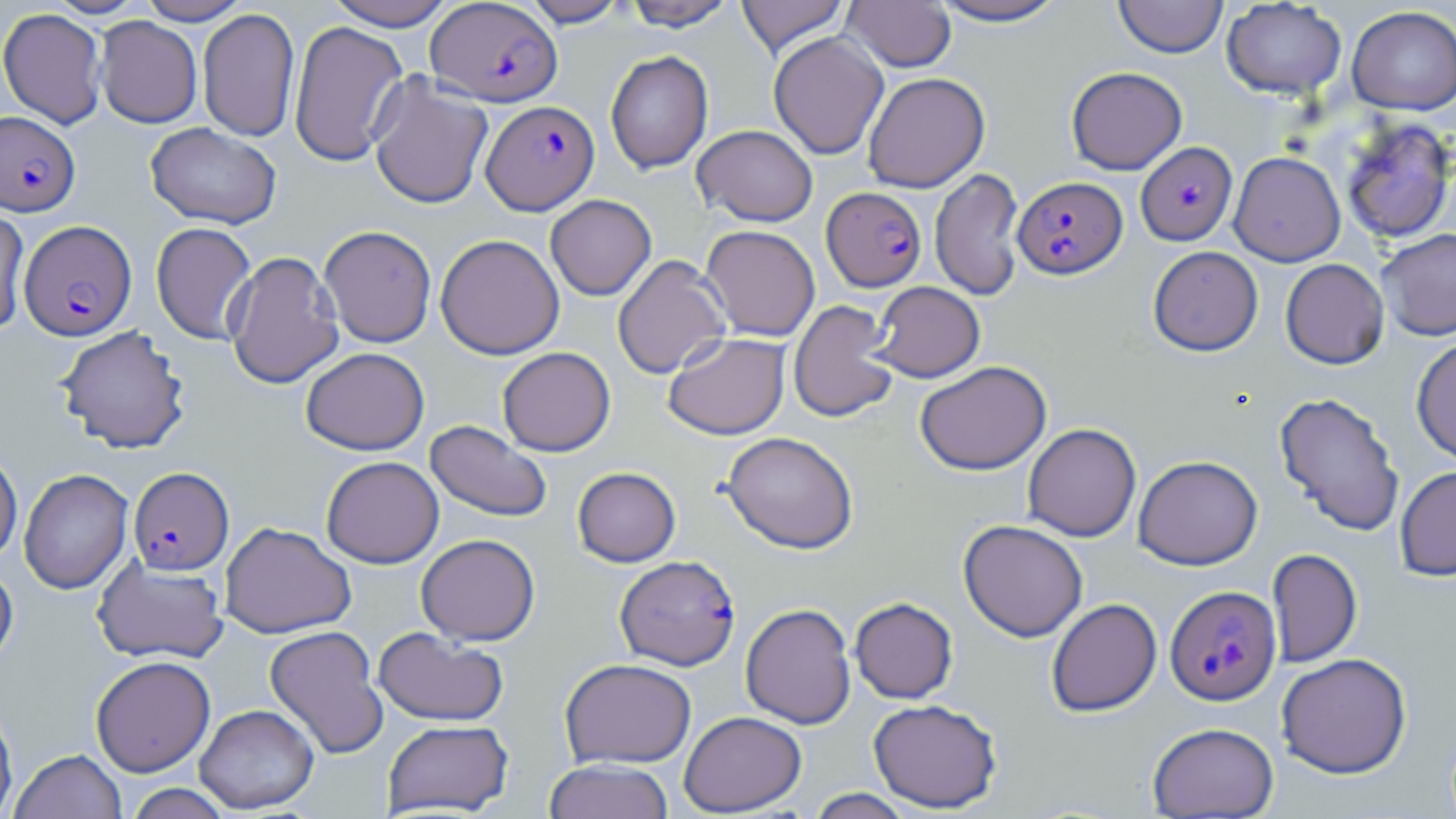

slide_level_diagnosis: Plasmodium falciparum
uninfected_red_blood_cell_locations: 'approximate bounding boxes as named x1/y1/x2/y2 corners in pixels: (x1=135, y1=0, x2=252, y2=25), (x1=324, y1=0, x2=459, y2=30), (x1=621, y1=0, x2=737, y2=30), (x1=736, y1=0, x2=850, y2=56), (x1=927, y1=0, x2=1071, y2=26), (x1=1113, y1=0, x2=1228, y2=58), (x1=521, y1=1, x2=630, y2=27), (x1=841, y1=1, x2=957, y2=73), (x1=1221, y1=1, x2=1347, y2=100), (x1=1347, y1=6, x2=1456, y2=115), (x1=0, y1=7, x2=107, y2=129), (x1=198, y1=8, x2=300, y2=142), (x1=95, y1=17, x2=202, y2=128), (x1=289, y1=20, x2=408, y2=166), (x1=768, y1=32, x2=889, y2=160), (x1=605, y1=50, x2=713, y2=173), (x1=1066, y1=67, x2=1187, y2=174), (x1=862, y1=72, x2=990, y2=193), (x1=368, y1=73, x2=493, y2=210), (x1=1340, y1=117, x2=1455, y2=243), (x1=145, y1=122, x2=282, y2=230), (x1=691, y1=124, x2=818, y2=226), (x1=1229, y1=151, x2=1345, y2=267), (x1=930, y1=168, x2=1025, y2=301), (x1=545, y1=194, x2=656, y2=300), (x1=0, y1=205, x2=30, y2=337), (x1=150, y1=222, x2=257, y2=345), (x1=319, y1=225, x2=437, y2=347), (x1=700, y1=225, x2=820, y2=342), (x1=1376, y1=228, x2=1456, y2=341), (x1=435, y1=233, x2=564, y2=359), (x1=1148, y1=246, x2=1263, y2=356), (x1=224, y1=251, x2=344, y2=389), (x1=612, y1=255, x2=731, y2=380), (x1=1280, y1=258, x2=1389, y2=369), (x1=869, y1=281, x2=985, y2=383), (x1=788, y1=300, x2=900, y2=423), (x1=55, y1=325, x2=191, y2=454), (x1=663, y1=332, x2=790, y2=440), (x1=1411, y1=336, x2=1456, y2=466), (x1=300, y1=347, x2=429, y2=455), (x1=497, y1=347, x2=615, y2=456), (x1=914, y1=361, x2=1051, y2=475), (x1=1274, y1=391, x2=1405, y2=536), (x1=425, y1=420, x2=552, y2=522), (x1=1023, y1=423, x2=1141, y2=542), (x1=721, y1=431, x2=859, y2=553), (x1=0, y1=447, x2=23, y2=565), (x1=1132, y1=455, x2=1263, y2=570), (x1=321, y1=456, x2=444, y2=568), (x1=1394, y1=465, x2=1456, y2=581), (x1=572, y1=466, x2=681, y2=567), (x1=19, y1=468, x2=133, y2=594), (x1=958, y1=519, x2=1088, y2=641), (x1=220, y1=521, x2=356, y2=638), (x1=416, y1=533, x2=540, y2=645), (x1=1267, y1=548, x2=1362, y2=667), (x1=92, y1=556, x2=230, y2=664), (x1=0, y1=560, x2=18, y2=671), (x1=849, y1=597, x2=958, y2=703), (x1=1046, y1=598, x2=1161, y2=716), (x1=740, y1=604, x2=856, y2=729), (x1=264, y1=625, x2=388, y2=759), (x1=373, y1=627, x2=509, y2=727), (x1=1276, y1=652, x2=1412, y2=778), (x1=90, y1=656, x2=216, y2=776), (x1=560, y1=658, x2=697, y2=768), (x1=0, y1=698, x2=18, y2=819), (x1=868, y1=698, x2=1003, y2=812), (x1=195, y1=703, x2=319, y2=814), (x1=679, y1=710, x2=807, y2=816), (x1=382, y1=719, x2=513, y2=816), (x1=1147, y1=721, x2=1279, y2=818), (x1=10, y1=749, x2=126, y2=819), (x1=544, y1=759, x2=674, y2=819), (x1=124, y1=783, x2=235, y2=818), (x1=806, y1=788, x2=914, y2=819)'
plasmodium_falciparum_infected_red_blood_cell_locations: 'approximate bounding boxes as named x1/y1/x2/y2 corners in pixels: (x1=426, y1=1, x2=562, y2=107), (x1=481, y1=100, x2=599, y2=215), (x1=1, y1=111, x2=80, y2=216), (x1=1135, y1=141, x2=1237, y2=246), (x1=1013, y1=176, x2=1127, y2=278), (x1=824, y1=184, x2=929, y2=289), (x1=19, y1=220, x2=137, y2=341), (x1=128, y1=467, x2=234, y2=575), (x1=614, y1=555, x2=740, y2=670), (x1=1165, y1=585, x2=1281, y2=705)'
image_size: 1456×819 pixels
stain: May-Grünwald-Giemsa
magnification: 1000x
field_of_view: one of a larger specimen
modality: optical microscopy
preparation: thin blood film